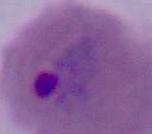
Summary:
  - Identification: Plasmodium
  - Modality: photomicrograph
  - Magnification: 400x or 1000x